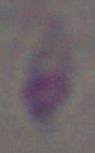

Toxoplasma gondii is shown. 1000x magnification. Micrograph.